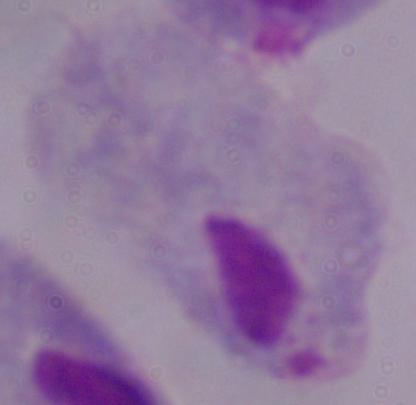
Captured at 1000x magnification. A trichomonad is shown. Photomicrograph.